Describe the morphology of the red blood cells.
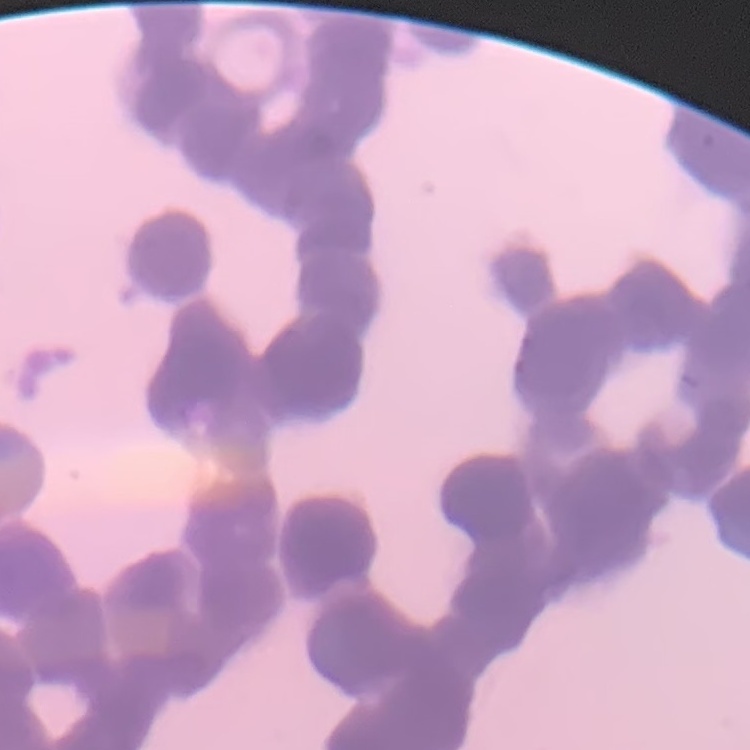
They show rouleaux formation.

Summary:
  - Image type: square crop of a larger photomicrograph
  - Preparation: thin peripheral smear
  - Stain: Field's or Giemsa